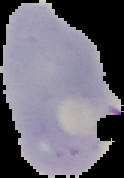
Malaria status: parasitized. Cell region segmented out of the field of view; the surrounding area is masked to black. Image is 124×178 pixels. From a thin blood smear.